Name the parasite shown.
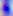
Toxoplasma gondii.

{
  "magnification": "400x",
  "modality": "photomicrograph"
}